Assess this cell for malaria.
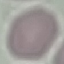

It is uninfected.

Acquired by smartphone through the microscope eyepiece. Thin smear of blood. Automatically extracted cell patch, resized to 64 × 64 pixels. Giemsa stain.